Look for Plasmodium parasites.
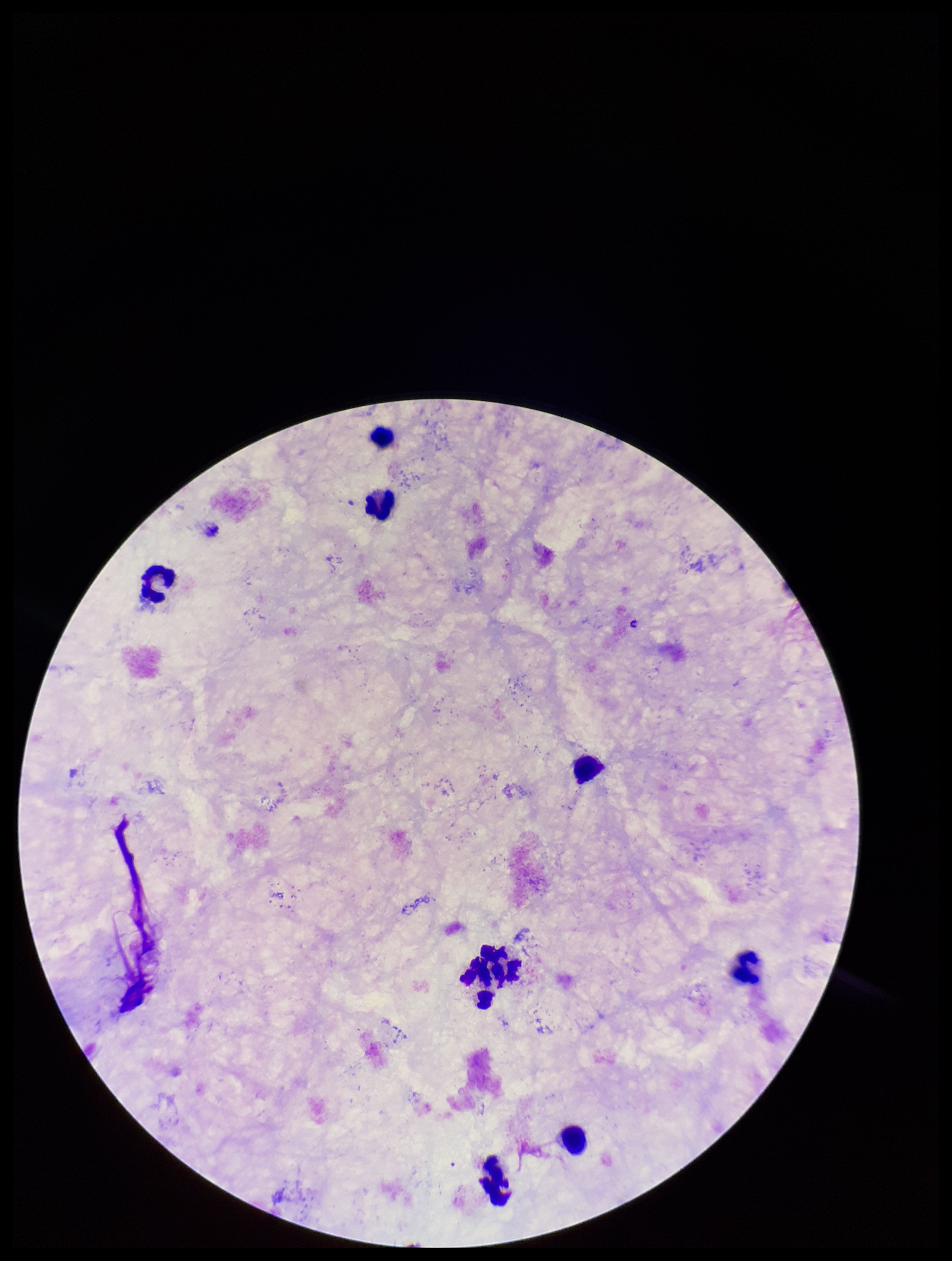
None seen.

image size = 952×1261 pixels
patient malaria status = negative
field of view = single
preparation = thick smear
leukocyte count = 9
parasite count = 0
capture = smartphone photograph through the microscope eyepiece
stain = Giemsa